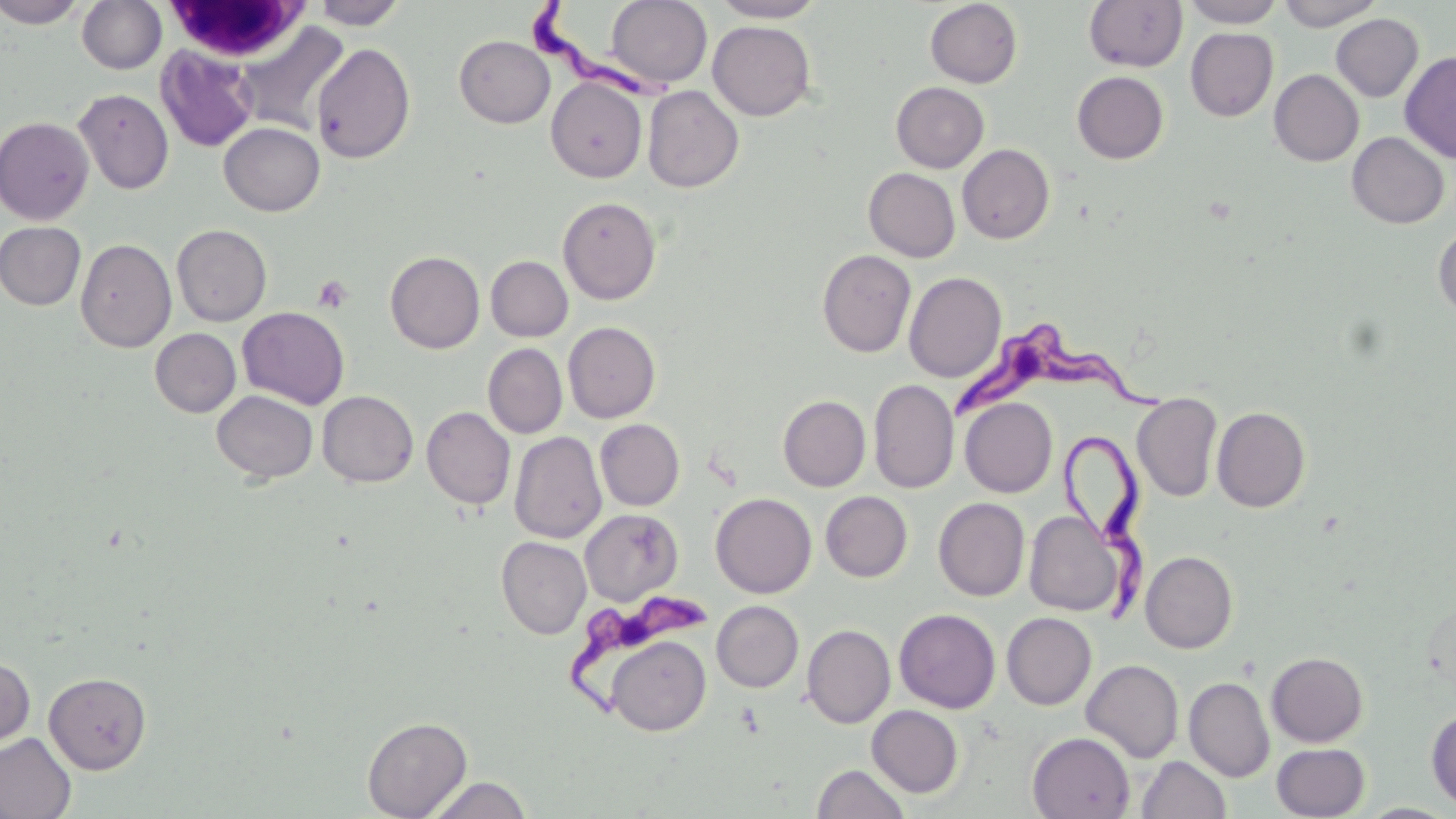
Approximate bounding boxes as named x1/y1/x2/y2 corners in pixels. Platelet locations: (x1=313, y1=275, x2=353, y2=314). Trypanosoma brucei locations: (x1=530, y1=6, x2=676, y2=104), (x1=953, y1=322, x2=1181, y2=416), (x1=1055, y1=428, x2=1161, y2=611), (x1=558, y1=582, x2=713, y2=723). White blood cell locations: (x1=163, y1=1, x2=312, y2=63). Uninfected red blood cell locations: (x1=1, y1=0, x2=87, y2=28), (x1=77, y1=0, x2=167, y2=74), (x1=311, y1=0, x2=408, y2=29), (x1=606, y1=0, x2=712, y2=88), (x1=710, y1=0, x2=826, y2=22), (x1=925, y1=0, x2=1023, y2=87), (x1=1084, y1=0, x2=1188, y2=71), (x1=1182, y1=0, x2=1284, y2=27), (x1=1277, y1=0, x2=1382, y2=30), (x1=1331, y1=14, x2=1423, y2=102), (x1=233, y1=21, x2=351, y2=135), (x1=708, y1=21, x2=815, y2=120), (x1=1185, y1=27, x2=1278, y2=121), (x1=454, y1=35, x2=555, y2=128), (x1=311, y1=42, x2=416, y2=163), (x1=155, y1=46, x2=259, y2=153), (x1=1399, y1=51, x2=1456, y2=163), (x1=1269, y1=69, x2=1364, y2=166), (x1=1072, y1=71, x2=1169, y2=164), (x1=546, y1=77, x2=647, y2=182), (x1=891, y1=82, x2=989, y2=173), (x1=642, y1=85, x2=744, y2=192), (x1=74, y1=88, x2=174, y2=194), (x1=0, y1=116, x2=95, y2=224), (x1=219, y1=122, x2=325, y2=216), (x1=1347, y1=132, x2=1450, y2=228), (x1=958, y1=144, x2=1054, y2=243), (x1=864, y1=168, x2=960, y2=262), (x1=558, y1=196, x2=660, y2=305), (x1=0, y1=221, x2=86, y2=310), (x1=172, y1=224, x2=272, y2=326), (x1=1433, y1=225, x2=1456, y2=320), (x1=75, y1=238, x2=176, y2=352), (x1=817, y1=249, x2=916, y2=357), (x1=385, y1=251, x2=485, y2=353), (x1=486, y1=256, x2=573, y2=341), (x1=904, y1=271, x2=1006, y2=382), (x1=238, y1=306, x2=350, y2=409), (x1=563, y1=322, x2=660, y2=423), (x1=150, y1=328, x2=241, y2=417), (x1=483, y1=343, x2=567, y2=438), (x1=869, y1=379, x2=959, y2=493), (x1=212, y1=390, x2=318, y2=483), (x1=317, y1=390, x2=419, y2=487), (x1=1132, y1=391, x2=1222, y2=502), (x1=778, y1=395, x2=871, y2=491), (x1=960, y1=397, x2=1057, y2=497), (x1=422, y1=406, x2=515, y2=509), (x1=1212, y1=406, x2=1310, y2=512), (x1=595, y1=419, x2=684, y2=510), (x1=509, y1=431, x2=607, y2=543), (x1=821, y1=491, x2=912, y2=581), (x1=710, y1=493, x2=816, y2=598), (x1=933, y1=497, x2=1030, y2=601), (x1=580, y1=509, x2=682, y2=605), (x1=1024, y1=511, x2=1127, y2=617), (x1=496, y1=536, x2=591, y2=639), (x1=1141, y1=550, x2=1237, y2=653), (x1=712, y1=601, x2=803, y2=692), (x1=894, y1=609, x2=1001, y2=713), (x1=1002, y1=612, x2=1096, y2=710), (x1=802, y1=624, x2=895, y2=728), (x1=606, y1=635, x2=710, y2=736), (x1=1266, y1=651, x2=1368, y2=747), (x1=0, y1=654, x2=35, y2=756), (x1=1081, y1=659, x2=1184, y2=763), (x1=44, y1=672, x2=151, y2=774), (x1=1184, y1=676, x2=1275, y2=782), (x1=867, y1=705, x2=963, y2=797), (x1=1426, y1=707, x2=1456, y2=810), (x1=362, y1=716, x2=472, y2=819), (x1=1027, y1=732, x2=1135, y2=819), (x1=0, y1=733, x2=76, y2=819), (x1=1272, y1=742, x2=1370, y2=819), (x1=1137, y1=755, x2=1231, y2=818), (x1=812, y1=764, x2=910, y2=819), (x1=426, y1=775, x2=532, y2=818). Slide-level diagnosis: Trypanosoma brucei. Single field of view. Optical microscopy. Thin blood film. Captured at 1000x magnification. Image is 1456×819 pixels. May-Grünwald-Giemsa stain.